Find the red blood cells and label each as Plasmodium falciparum-infected, uninfected, or of indeterminate infection status.
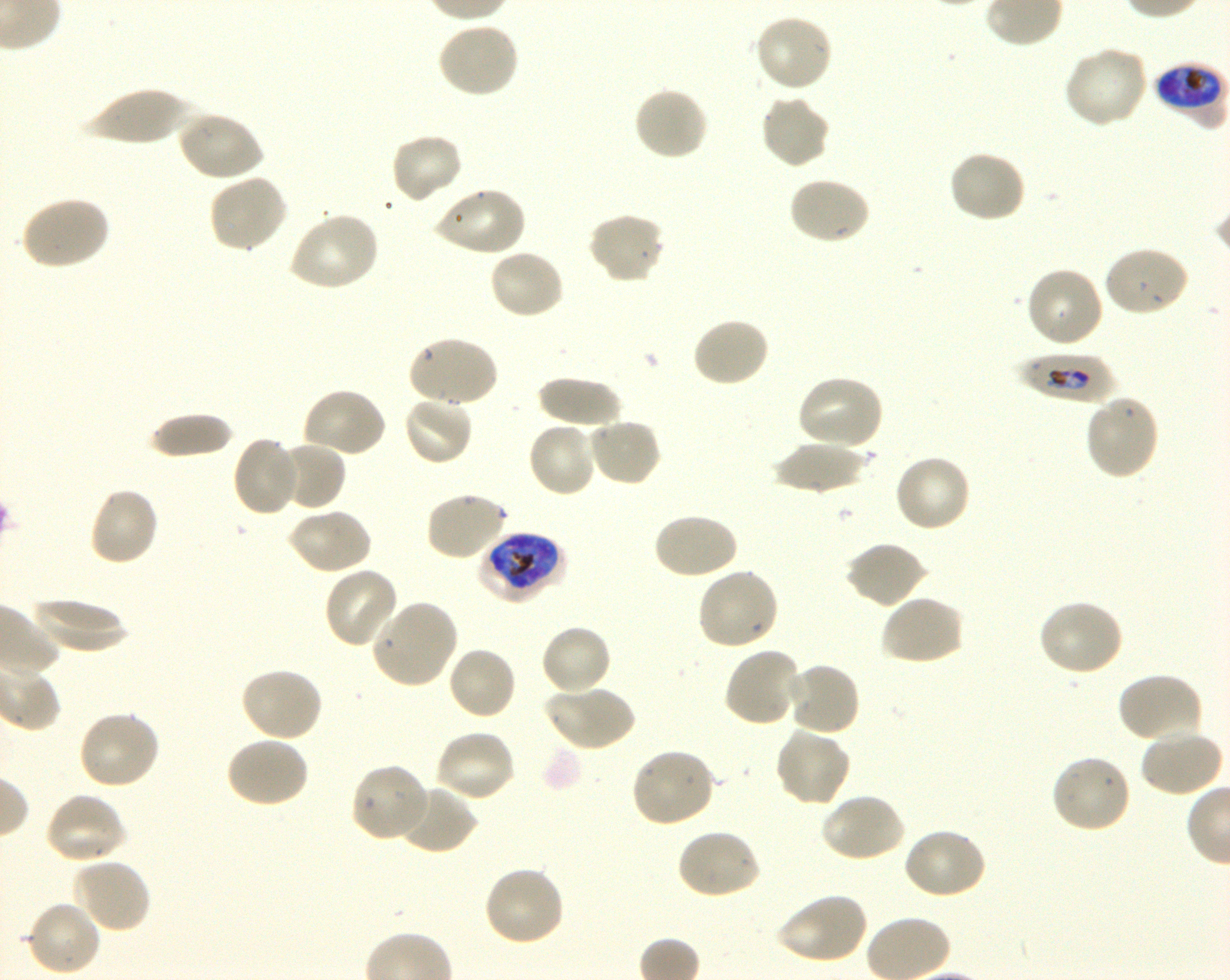

Approximate bounding boxes as [x1, y1, x2, y2] in pixels. Not every red blood cell is marked. A life-cycle stage — or a range of stages, where the recorded stages span more than one — follows each staged infected red blood cell.
Infected red blood cells: [1153, 63, 1226, 122] early trophozoite to early schizont; [1015, 352, 1118, 404] late ring to early trophozoite; [478, 531, 565, 604] late trophozoite to early schizont.
Uninfected red blood cells: [754, 13, 834, 94], [436, 22, 520, 100], [1063, 44, 1149, 128], [633, 86, 709, 161], [80, 87, 195, 146], [759, 94, 832, 169], [177, 110, 264, 182], [389, 132, 464, 205], [947, 150, 1026, 225], [207, 173, 289, 255], [787, 175, 871, 245], [432, 185, 527, 256], [17, 195, 110, 271], [287, 211, 380, 293], [587, 211, 667, 285], [1102, 245, 1190, 317], [487, 248, 565, 321], [1024, 266, 1105, 350], [691, 317, 770, 389], [406, 335, 498, 409], [795, 374, 885, 452], [535, 376, 625, 427], [301, 387, 387, 460], [1084, 394, 1161, 481], [402, 395, 474, 467], [146, 413, 235, 460], [588, 417, 663, 488], [527, 421, 600, 498], [231, 435, 299, 517], [274, 440, 346, 512], [770, 442, 870, 495], [893, 454, 972, 534], [87, 486, 160, 568], [424, 490, 510, 562], [286, 507, 373, 576], [652, 511, 738, 580], [845, 540, 928, 609], [323, 566, 400, 650], [696, 567, 780, 652], [880, 595, 965, 667], [29, 598, 130, 652], [370, 598, 459, 689], [1037, 599, 1126, 677], [540, 624, 612, 696], [447, 645, 519, 721], [723, 646, 802, 728], [784, 661, 861, 738], [239, 667, 324, 743], [1116, 672, 1204, 745], [544, 683, 635, 753], [77, 708, 161, 790], [773, 728, 851, 808], [1139, 728, 1224, 797], [433, 729, 516, 804], [225, 736, 310, 808], [629, 748, 716, 828], [1051, 752, 1132, 834], [349, 762, 431, 843], [397, 782, 477, 855], [43, 792, 126, 865], [820, 792, 906, 863], [676, 827, 763, 901], [901, 827, 987, 900], [71, 857, 151, 934], [482, 864, 565, 947], [775, 891, 869, 965], [25, 899, 102, 977].
No red blood cells of indeterminate infection status observed.

stain = Giemsa
image size = 1230×980 pixels
culture = Plasmodium falciparum strain 3D7, shaking, in vitro
preparation = thin blood film
donor blood group = O+
field of view = one from this slide
objective = 100x, oil immersion, numerical aperture 1.30